Assess this cell for malaria.
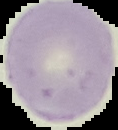

It is uninfected.

The area outside the segmented cell region is set to black. From a thin blood film. Image is 118×130 pixels.